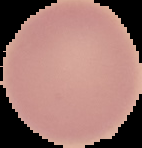

Result: no Plasmodium parasites detected. The area outside the segmented cell region is set to black. Image is 142×148 pixels. From a thin blood film.